State which cell type is depicted.
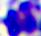
A leukocyte.

Photomicrograph. 400x magnification.